Identify the parasite.
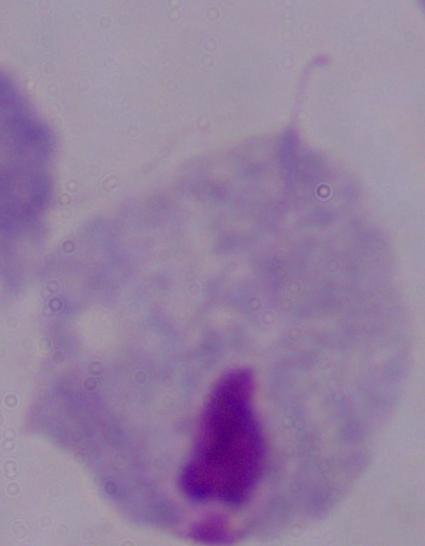

A trichomonad.

Summary:
  - Modality: photomicrograph
  - Magnification: 1000x